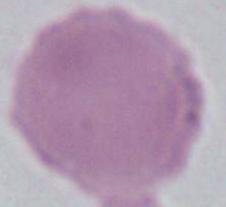

magnification = 1000x
modality = micrograph
identification = erythrocyte